Give the position of every leukocyte visible.
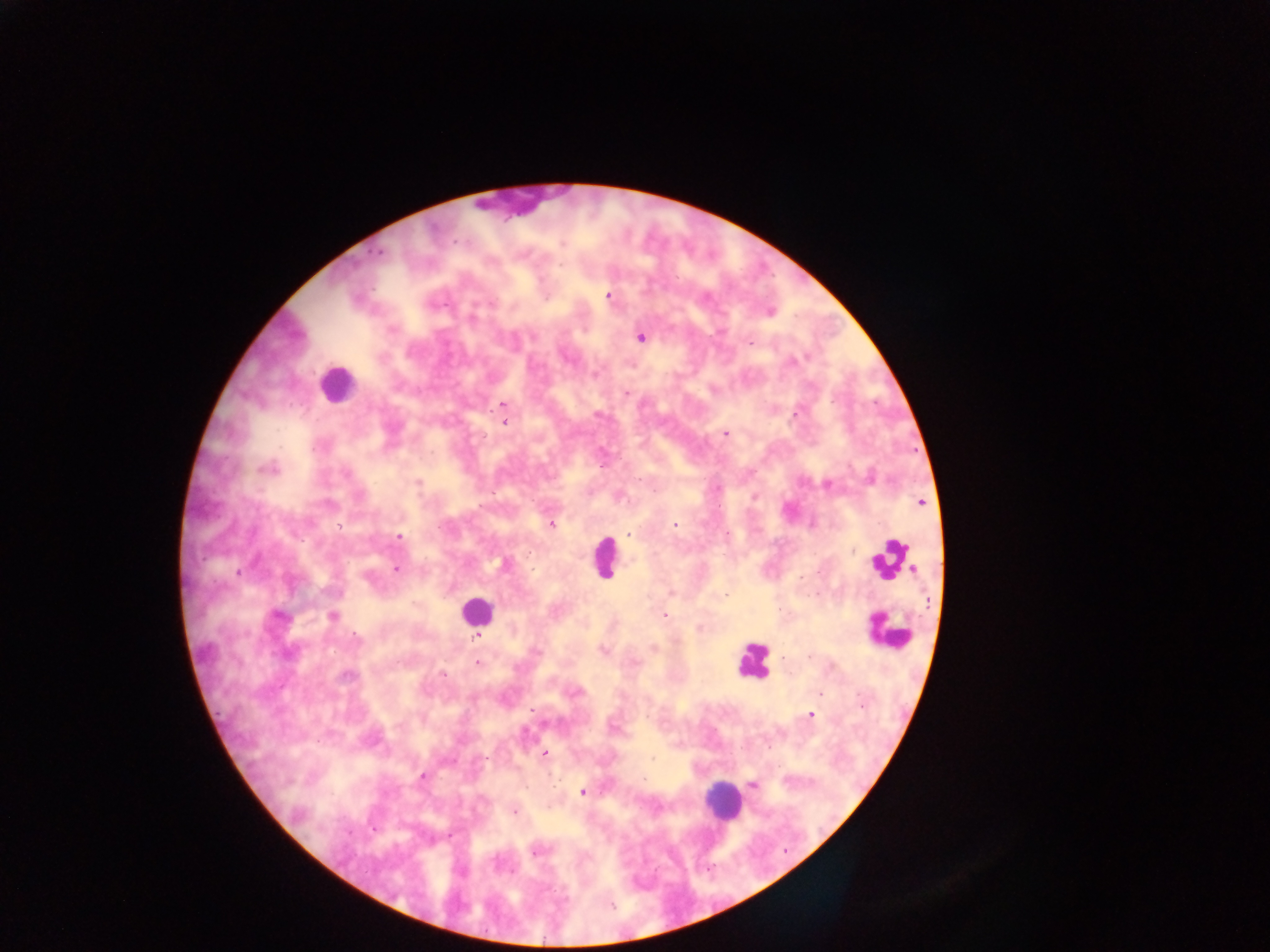
Approximate centers as x y in pixels.
Leukocytes: 515 202; 336 383; 604 558; 889 559; 476 611; 887 632; 753 660; 723 802.

image size = 1270×952 pixels
Plasmodium parasite locations = approximate centers as x y in pixels: 378 252; 608 296; 768 311; 641 336; 749 343; 791 360; 625 392; 503 404; 795 413; 503 422; 725 433; 266 468; 418 482; 827 484; 756 496; 919 502; 551 524; 675 525; 629 533; 399 537; 504 565; 396 568; 671 592; 277 615; 663 615; 333 616; 699 629; 476 637; 653 648; 602 649; 477 663; 346 675; 819 694; 861 703; 810 715; 544 754; 752 784; 582 791; 513 811; 449 835; 536 849; 611 904
capture = mobile-phone photograph through a microscope
field of view = single
preparation = thick blood film
country = Ghana